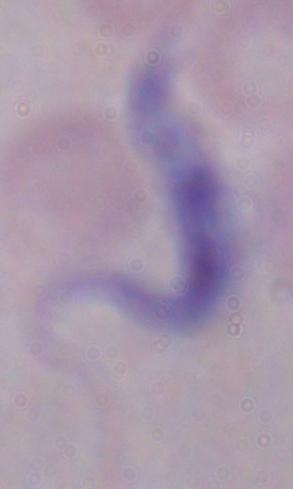

Photomicrograph. Captured at 1000x magnification. A trypanosome is shown.